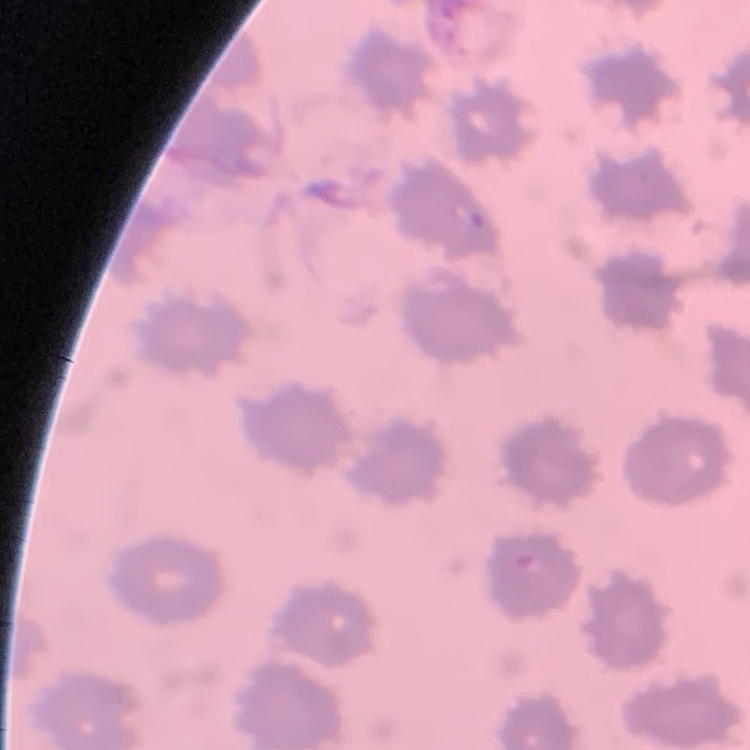

Summary:
  - Erythrocyte morphology: no rouleaux formation
  - Preparation: thin peripheral smear
  - Stain: Field's or Giemsa
  - Image type: one tile cut from a larger photomicrograph